Report the malaria status of this cell.
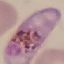

Parasitized.

Cell patch, automatically extracted from a larger field of view and resized to 64 × 64 pixels. Thin blood smear. Giemsa-stained preparation. Acquired by smartphone through the microscope eyepiece.